Assess the morphology of the erythrocytes.
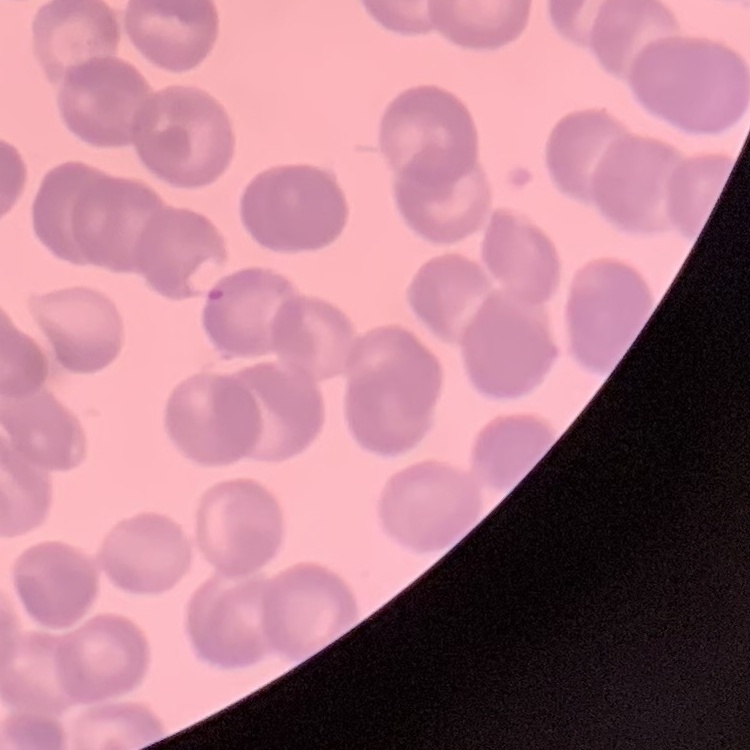

Rouleaux formation.

Summary:
  - Stain: Field's or Giemsa
  - Preparation: thin blood smear
  - Image type: one tile cut from a larger photomicrograph